Locate platelets.
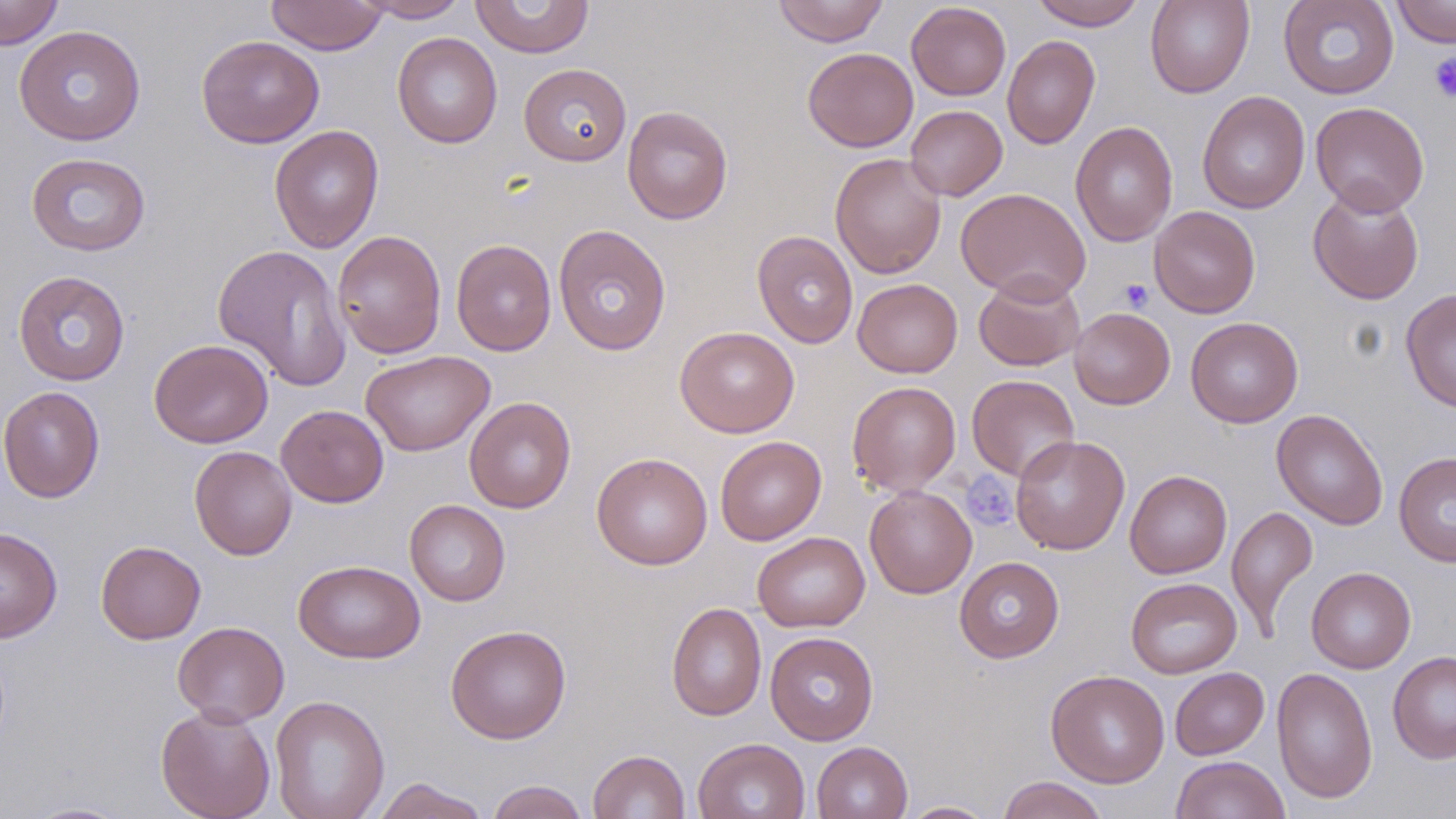
Approximate bounding boxes as [x1, y1, x2, y2] in pixels.
Platelets: [1429, 51, 1456, 103], [1119, 279, 1154, 312], [961, 472, 1017, 530].

Uninfected red blood cell locations: [0, 0, 64, 50], [266, 0, 388, 55], [356, 0, 472, 22], [773, 0, 888, 46], [1030, 0, 1146, 31], [1145, 0, 1254, 98], [1278, 0, 1400, 100], [1391, 0, 1456, 47], [470, 1, 595, 58], [906, 2, 1011, 101], [14, 25, 146, 145], [392, 31, 503, 149], [195, 34, 325, 149], [1002, 35, 1100, 150], [803, 47, 918, 152], [519, 63, 632, 166], [1197, 90, 1310, 214], [1310, 101, 1430, 216], [622, 105, 733, 224], [905, 105, 1007, 201], [1070, 121, 1178, 246], [269, 124, 385, 253], [26, 152, 151, 256], [829, 152, 946, 279], [1308, 186, 1425, 304], [955, 187, 1091, 304], [1149, 205, 1260, 318], [553, 223, 671, 356], [332, 230, 447, 359], [752, 230, 858, 348], [451, 239, 557, 356], [213, 244, 352, 392], [13, 270, 131, 386], [973, 273, 1085, 371], [852, 278, 962, 377], [1400, 287, 1456, 412], [1069, 307, 1175, 409], [1185, 317, 1303, 428], [675, 326, 799, 438], [149, 338, 273, 448], [360, 350, 495, 457], [966, 374, 1080, 482], [847, 381, 961, 495], [0, 386, 105, 503], [463, 396, 576, 514], [276, 404, 389, 507], [1271, 409, 1388, 530], [1010, 434, 1130, 555], [715, 436, 826, 545], [189, 445, 297, 560], [591, 452, 713, 570], [1394, 452, 1456, 567], [1125, 470, 1232, 579], [864, 485, 977, 599], [405, 500, 510, 606], [1226, 504, 1319, 640], [0, 526, 63, 643], [752, 531, 870, 632], [96, 540, 206, 644], [954, 556, 1064, 663], [293, 559, 426, 664], [1307, 567, 1415, 673], [1126, 577, 1242, 678], [666, 602, 767, 722], [172, 621, 290, 726], [446, 624, 572, 744], [765, 631, 879, 745], [1388, 650, 1456, 764], [1272, 666, 1378, 804], [1170, 667, 1269, 760], [1045, 669, 1170, 788], [270, 694, 390, 819], [156, 705, 276, 819], [693, 737, 810, 819], [811, 741, 912, 819], [587, 749, 690, 819], [1170, 755, 1290, 819], [997, 776, 1109, 819], [370, 777, 491, 819], [486, 780, 590, 819], [897, 800, 999, 818], [21, 801, 134, 818]. Slide-level diagnosis: negative for blood parasites. May-Grünwald-Giemsa stain. Image is 1456×819 pixels. One field of a larger specimen. Thin blood film. Captured at 1000x magnification. Optical microscopy.